Assess this cell for malaria.
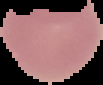
It is uninfected.

Summary:
  - Image size: 103×85 pixels
  - Image type: segmented cell region on a black background
  - Preparation: thin blood smear